Give the position of each Plasmodium falciparum parasite with its life-cycle stage, each leukocyte, and any debris.
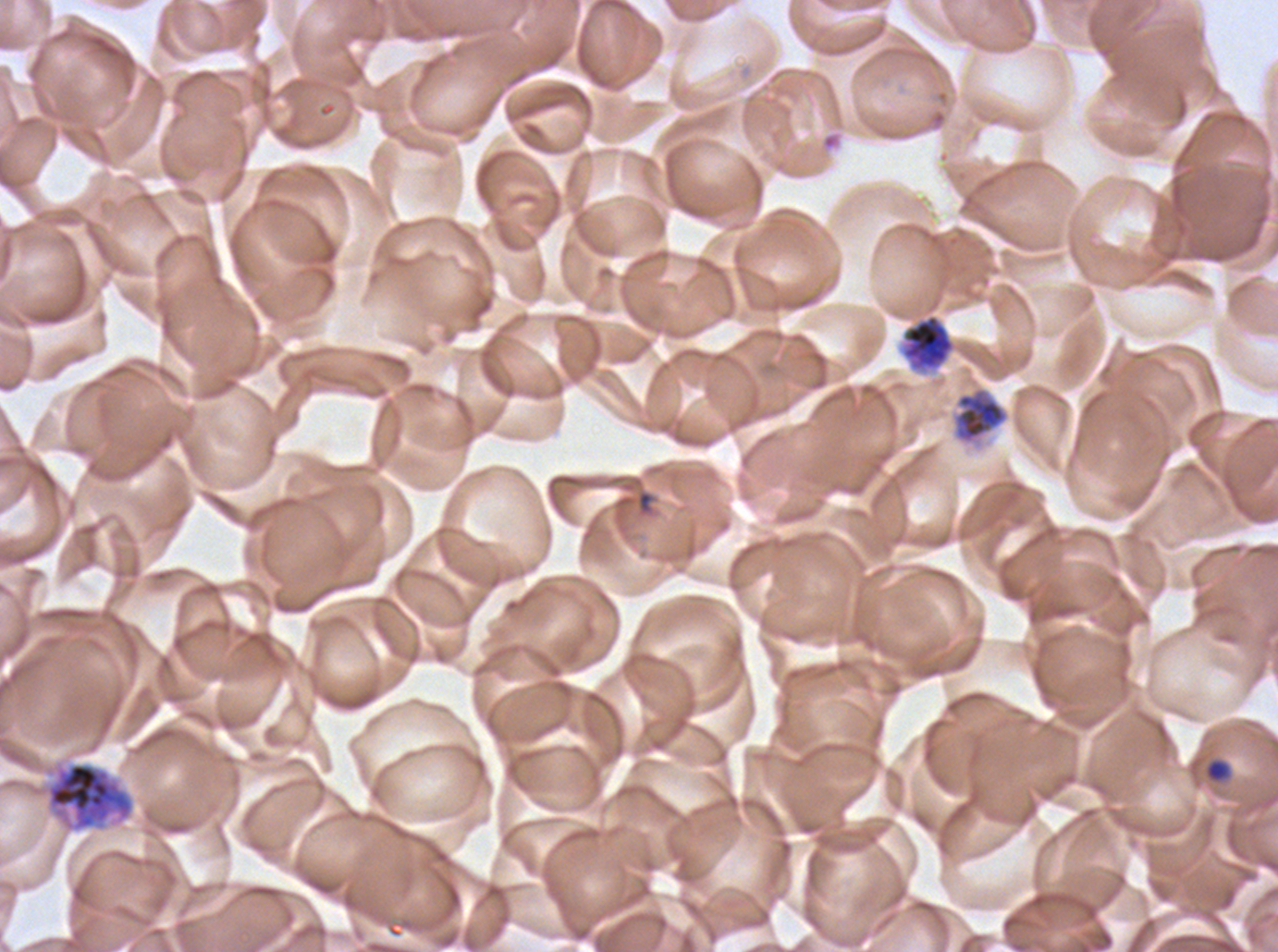

Approximate bounding boxes as {x1, y1, x2, y2} in pixels.
Rings: {614, 488, 657, 518}.
Late-ring/early-trophozoite forms: {1203, 757, 1232, 784}.
Late trophozoites: {950, 384, 1011, 450}.
Early schizonts: {901, 313, 956, 372}, {44, 762, 135, 833}.
No mid trophozoites, late schizonts, segmenters, gametocytes, leukocytes, or debris observed.

preparation = thin blood smear
image size = 1278×952 pixels
life-cycle stages observed = ring, late-ring/early-trophozoite, late trophozoite, early schizont
specimen = Plasmodium falciparum from a patient in The Gambia, cultured ex vivo for 24 to 48 hours
field of view = one sub-image of a larger composite
stain = Giemsa